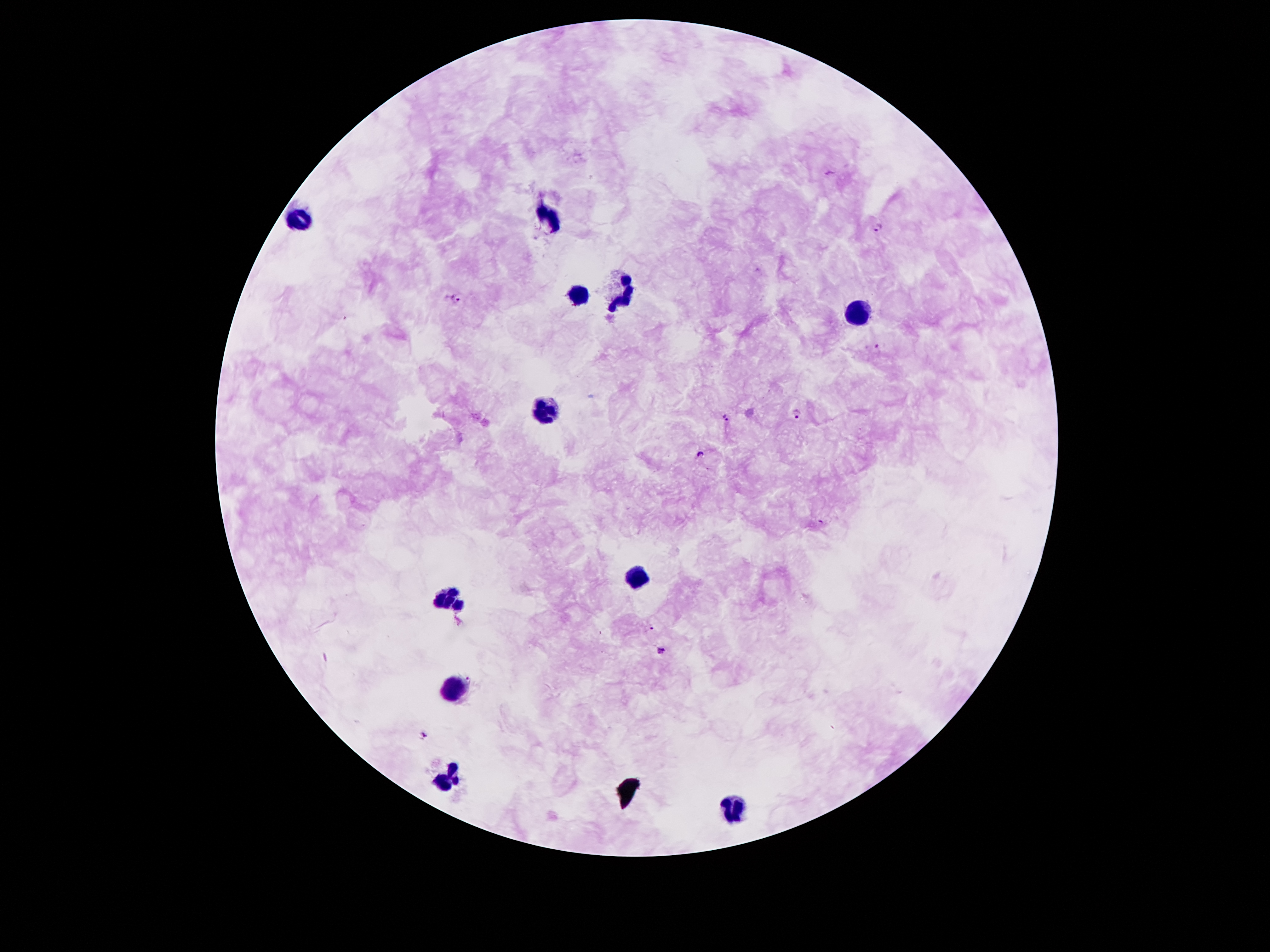
Approximate centers as {x, y} in pixels. Leukocyte locations: {548, 218}, {298, 219}, {575, 293}, {625, 294}, {857, 314}, {544, 409}, {639, 580}, {446, 598}, {455, 686}, {446, 775}, {737, 808}. Plasmodium parasite locations: {878, 226}, {457, 298}, {879, 345}, {798, 413}, {727, 418}, {701, 454}, {652, 627}, {664, 650}, {469, 678}, {427, 734}. Image is 1270×952 pixels. Single field of view. Smartphone photograph taken through the microscope eyepiece. Patient malaria status: positive for Plasmodium falciparum. Thick blood film. Giemsa stain. 100x magnification.